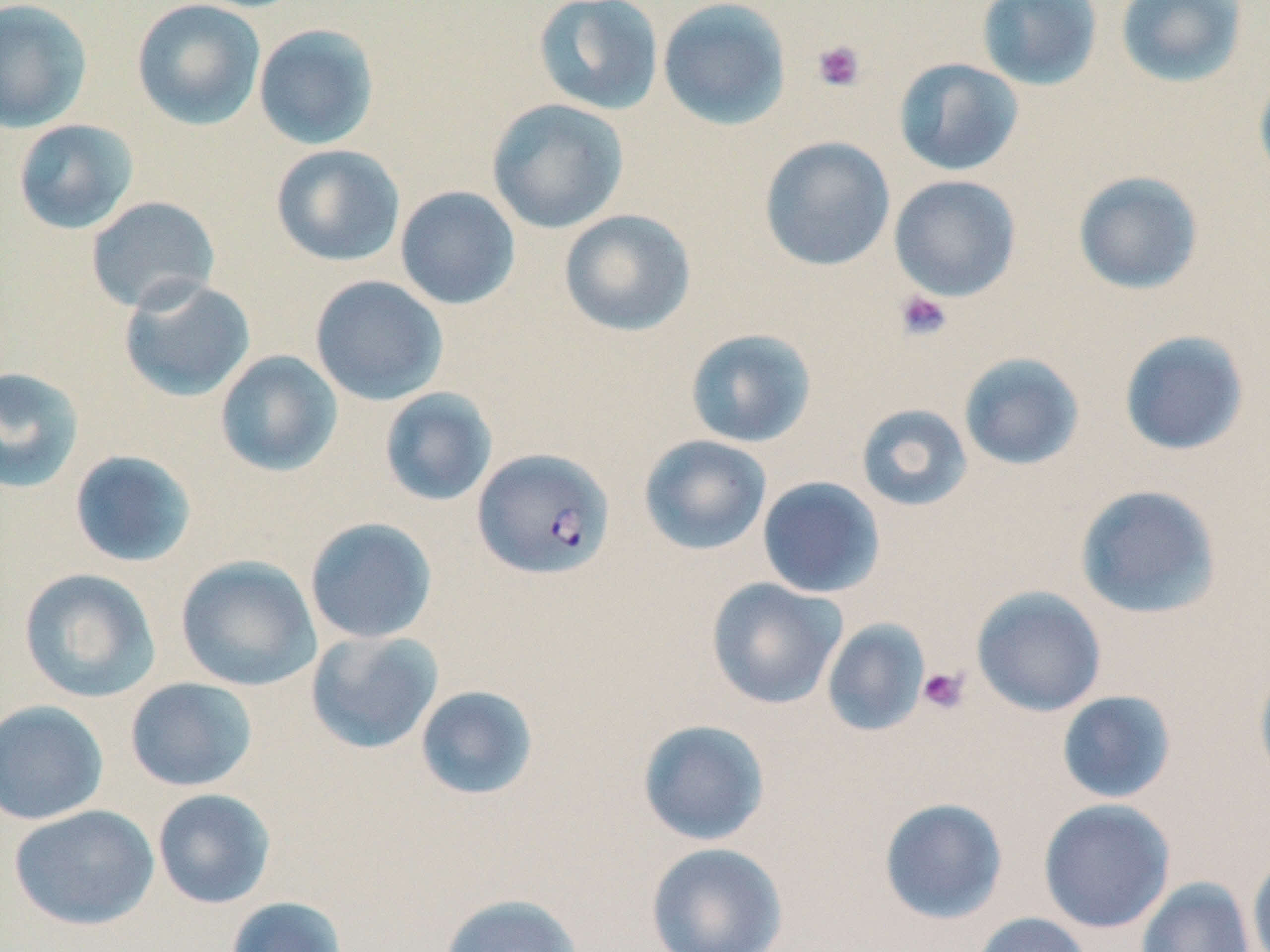
slide-level diagnosis = Plasmodium falciparum
preparation = thin blood film
stain = May-Grünwald-Giemsa
platelet locations = approximate bounding boxes as (x1,y1)-(x2,y2) corner pairs in pixels: (811,39)-(866,92), (894,290)-(952,341), (917,666)-(970,714)
image size = 1270×952 pixels
modality = optical microscopy
Plasmodium falciparum-infected red blood cell locations = approximate bounding boxes as (x1,y1)-(x2,y2) corner pairs in pixels: (473,447)-(614,581)
uninfected red blood cell locations = approximate bounding boxes as (x1,y1)-(x2,y2) corner pairs in pixels: (0,0)-(93,134), (131,0)-(266,131), (533,0)-(664,116), (657,0)-(792,131), (976,0)-(1104,90), (1115,0)-(1250,88), (253,23)-(381,150), (893,57)-(1024,177), (1253,66)-(1270,188), (487,98)-(630,234), (13,118)-(139,235), (759,136)-(895,272), (270,144)-(405,267), (1073,170)-(1205,296), (888,174)-(1021,302), (395,186)-(521,310), (85,196)-(221,314), (558,209)-(696,337), (309,275)-(448,405), (118,276)-(256,402), (684,328)-(817,449), (1118,330)-(1250,457), (214,350)-(343,477), (958,352)-(1086,472), (0,366)-(86,494), (378,387)-(498,507), (855,404)-(973,512), (638,434)-(772,556), (68,450)-(199,568), (757,476)-(886,598), (1074,484)-(1223,620), (304,517)-(438,644), (175,555)-(321,692), (18,567)-(161,703), (706,578)-(847,710), (971,586)-(1107,717), (821,619)-(931,737), (305,630)-(444,754), (1254,657)-(1270,790), (125,677)-(258,792), (414,685)-(539,801), (1056,690)-(1177,805), (0,699)-(109,826), (637,719)-(770,846), (152,789)-(276,909), (878,797)-(1008,925), (1038,798)-(1176,933), (8,804)-(159,931), (645,841)-(789,952), (1247,848)-(1270,952), (1135,877)-(1257,952), (437,893)-(584,952), (226,896)-(349,952), (971,912)-(1093,952)
magnification = 1000x
field of view = one of a larger specimen